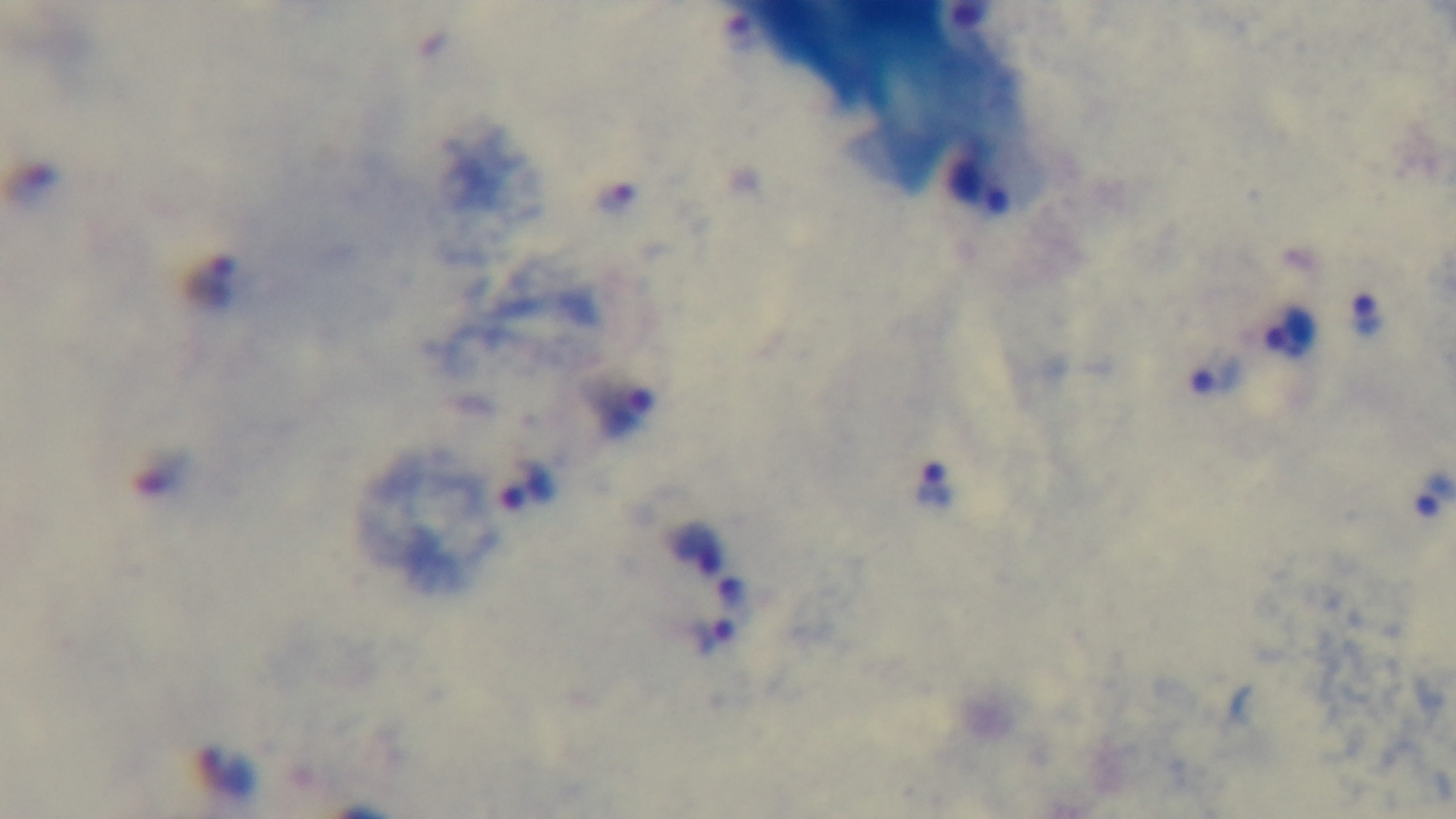
Giemsa-stained. Single field of view. 100x oil-immersion objective. Mounted 4K digital camera. Light microscopy. Malaria status: positive. Preparation: thick blood film.